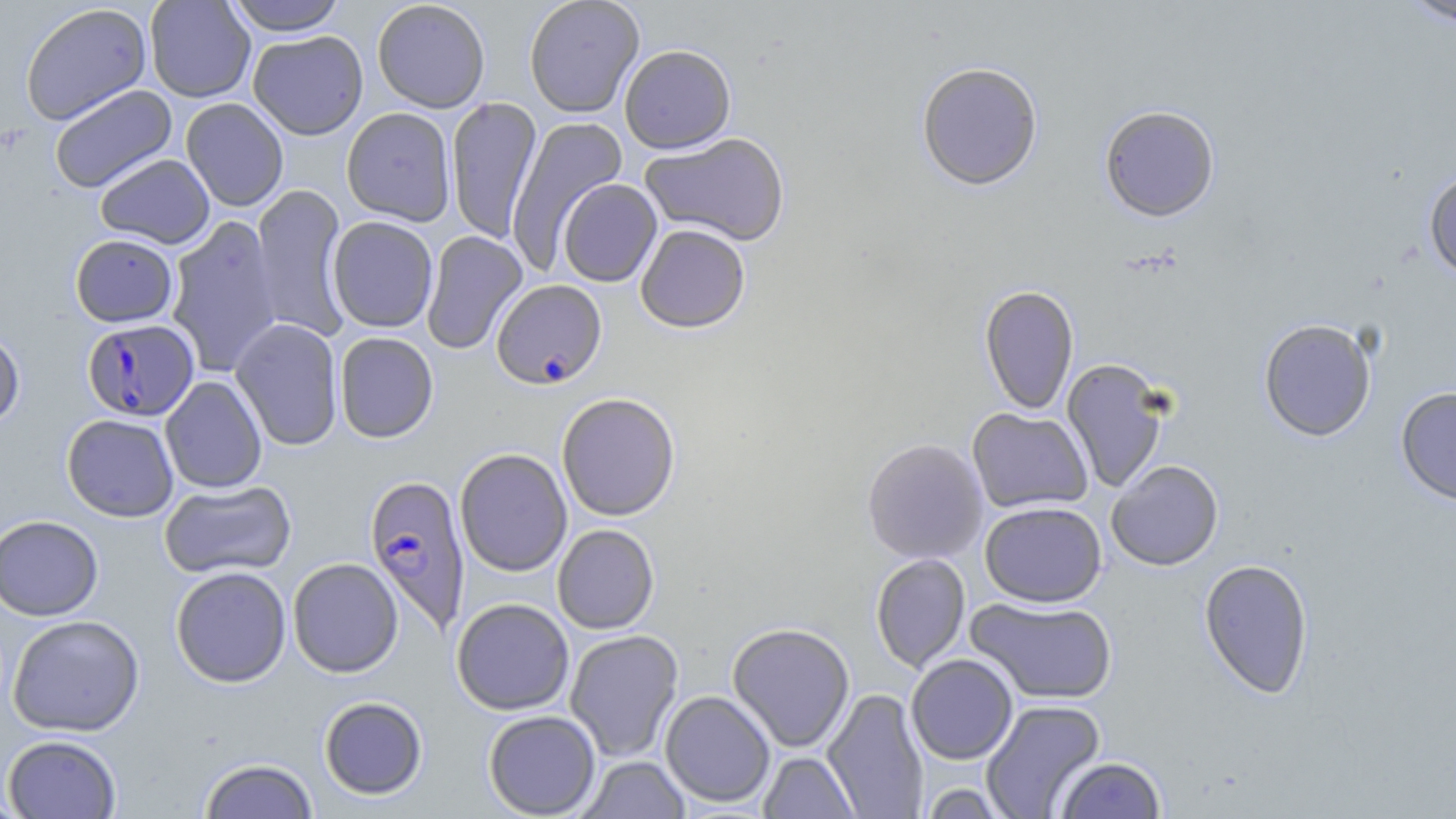
Approximate bounding boxes as [x1, y1, x2, y2] in pixels. Plasmodium falciparum-infected red blood cell locations: [491, 279, 608, 389], [81, 318, 199, 422], [364, 475, 471, 635]. Uninfected red blood cell locations: [144, 0, 256, 102], [224, 0, 348, 35], [524, 0, 645, 118], [1399, 0, 1456, 30], [372, 1, 490, 112], [19, 3, 152, 125], [248, 30, 368, 140], [619, 44, 736, 154], [916, 63, 1043, 191], [49, 84, 177, 194], [446, 96, 543, 244], [181, 98, 289, 212], [1099, 105, 1220, 223], [341, 107, 456, 226], [506, 116, 627, 274], [639, 132, 791, 247], [94, 153, 215, 249], [1423, 168, 1456, 281], [557, 179, 662, 287], [251, 185, 351, 341], [327, 216, 438, 333], [166, 217, 282, 378], [635, 224, 751, 333], [421, 231, 528, 355], [70, 234, 179, 327], [979, 285, 1079, 415], [229, 318, 344, 451], [1258, 318, 1377, 442], [0, 327, 25, 432], [334, 332, 439, 443], [1061, 358, 1172, 494], [160, 376, 268, 493], [1396, 387, 1456, 506], [556, 392, 680, 521], [967, 407, 1092, 514], [62, 414, 179, 522], [862, 438, 988, 564], [455, 448, 572, 577], [1106, 459, 1224, 571], [159, 479, 297, 580], [979, 501, 1107, 607], [0, 515, 103, 620], [552, 524, 659, 634], [870, 554, 970, 673], [287, 557, 403, 677], [1198, 558, 1314, 699], [170, 566, 291, 687], [966, 597, 1118, 705], [452, 598, 574, 715], [7, 614, 145, 736], [727, 622, 855, 752], [564, 629, 684, 762], [906, 654, 1018, 764], [822, 688, 929, 818], [660, 690, 776, 807], [318, 696, 428, 800], [981, 700, 1106, 819], [483, 710, 601, 818], [2, 734, 122, 818], [758, 751, 861, 818], [1054, 756, 1167, 818], [198, 757, 319, 818], [577, 757, 692, 818], [917, 783, 1013, 818], [0, 793, 32, 818]. Slide-level diagnosis: Plasmodium falciparum. Single field of view. Optical microscopy. Image is 1456×819 pixels. Captured at 1000x magnification. Thin blood film. May-Grünwald-Giemsa stain.